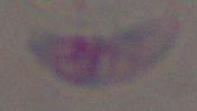

Photomicrograph. Toxoplasma gondii is shown. 1000x magnification.